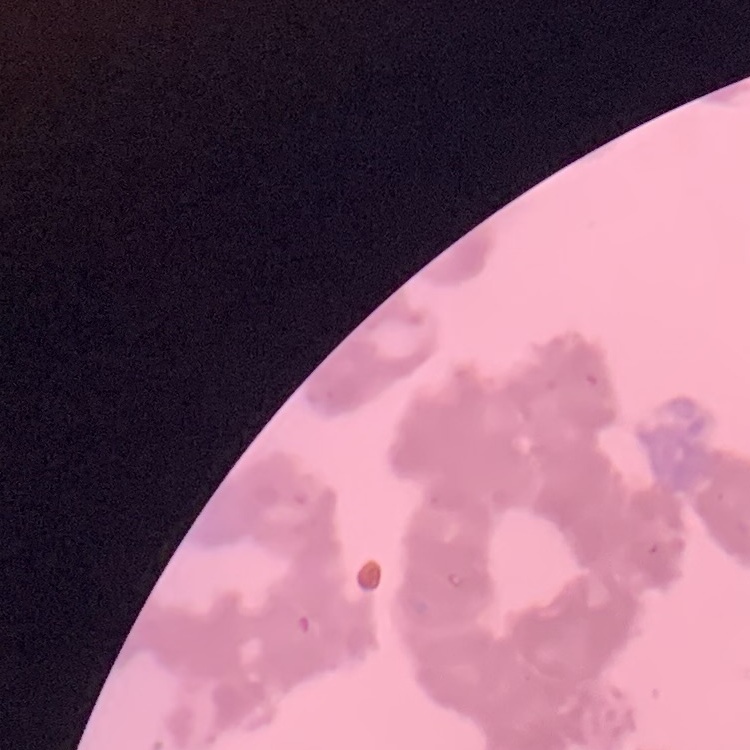

The red blood cells show rouleaux formation. One tile cut from a larger photomicrograph. Stained with either Field's or Giemsa. Thin blood film.